Locate every blood parasite and identify its species.
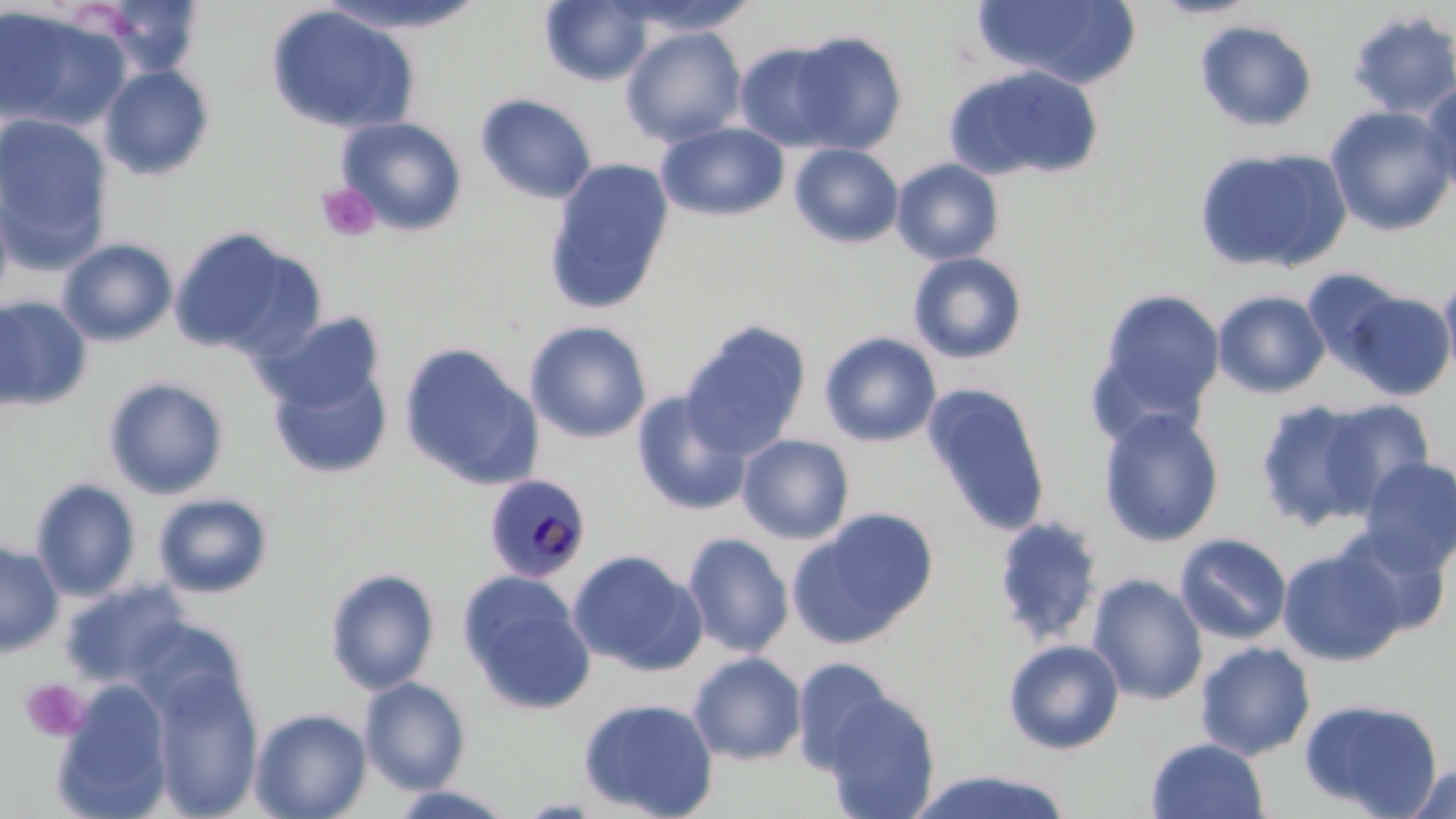
Approximate bounding boxes as (x1,y1)-(x2,y2) corner pairs in pixels.
Plasmodium malariae-infected red blood cells: (484,472)-(592,583).
No Plasmodium falciparum, Plasmodium ovale, Plasmodium vivax, Babesia divergens, or Trypanosoma brucei observed.

{
  "slide_level_diagnosis": "Plasmodium malariae",
  "uninfected_red_blood_cell_locations": "approximate bounding boxes as (x1,y1)-(x2,y2) corner pairs in pixels: (100,0)-(205,78), (316,0)-(488,34), (540,0)-(653,86), (612,0)-(760,37), (972,0)-(1140,89), (1149,0)-(1264,20), (265,5)-(419,135), (0,7)-(125,132), (1346,9)-(1456,121), (1194,19)-(1318,132), (621,25)-(748,147), (788,30)-(908,154), (733,41)-(849,151), (99,64)-(216,180), (944,64)-(1104,183), (1420,83)-(1456,195), (476,93)-(598,204), (1326,104)-(1456,236), (0,113)-(112,250), (336,116)-(469,236), (656,121)-(790,222), (789,143)-(904,248), (1193,147)-(1352,273), (543,158)-(675,314), (892,158)-(1005,265), (0,196)-(13,310), (168,226)-(322,361), (57,238)-(178,347), (908,252)-(1029,364), (1302,267)-(1407,373), (1440,273)-(1456,386), (1093,288)-(1226,426), (1213,290)-(1330,398), (1342,290)-(1455,400), (0,297)-(92,412), (258,310)-(387,414), (524,320)-(652,444), (681,320)-(812,458), (818,331)-(942,447), (398,343)-(543,490), (268,364)-(392,480), (103,377)-(229,499), (922,382)-(1052,538), (631,391)-(752,516), (1254,397)-(1381,531), (1316,399)-(1435,513), (1098,408)-(1225,547), (737,434)-(855,544), (1358,457)-(1456,576), (30,478)-(140,601), (153,492)-(274,599), (789,509)-(939,645), (992,515)-(1105,646), (1339,528)-(1452,637), (682,532)-(794,656), (1175,532)-(1292,644), (0,540)-(64,657), (1277,548)-(1407,666), (568,549)-(706,676), (325,568)-(440,695), (458,572)-(596,715), (1087,573)-(1208,705), (59,580)-(194,689), (1002,639)-(1125,755), (1196,640)-(1315,760), (688,651)-(807,765), (791,656)-(900,772), (150,667)-(264,819), (360,677)-(471,793), (51,682)-(174,819), (819,689)-(941,819), (577,696)-(720,819), (1299,697)-(1445,817), (249,708)-(372,819), (1146,737)-(1269,819), (1404,763)-(1456,819), (908,768)-(1075,819), (385,785)-(518,819)",
  "modality": "light microscopy",
  "platelet_locations": "approximate bounding boxes as (x1,y1)-(x2,y2) corner pairs in pixels: (316,181)-(381,243), (20,678)-(91,742)",
  "stain": "May-Grünwald-Giemsa",
  "image_size": "1456×819 pixels",
  "field_of_view": "single",
  "preparation": "thin blood smear",
  "magnification": "1000x"
}